Assess the morphology of the red blood cells.
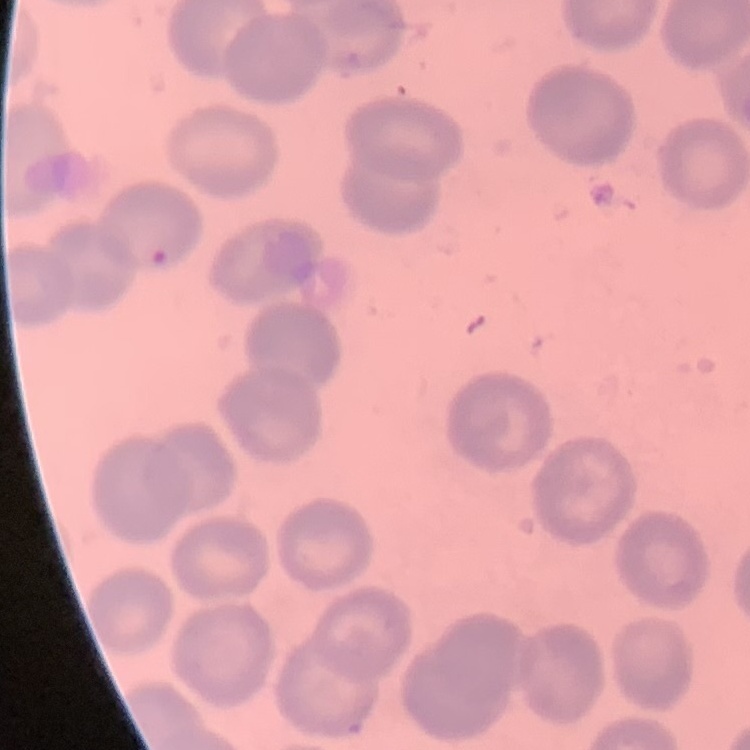

No rouleaux formation.

Summary:
  - Stain: Field's or Giemsa
  - Preparation: thin blood smear
  - Image type: square crop of a larger photomicrograph